Comment on the morphology of the erythrocytes.
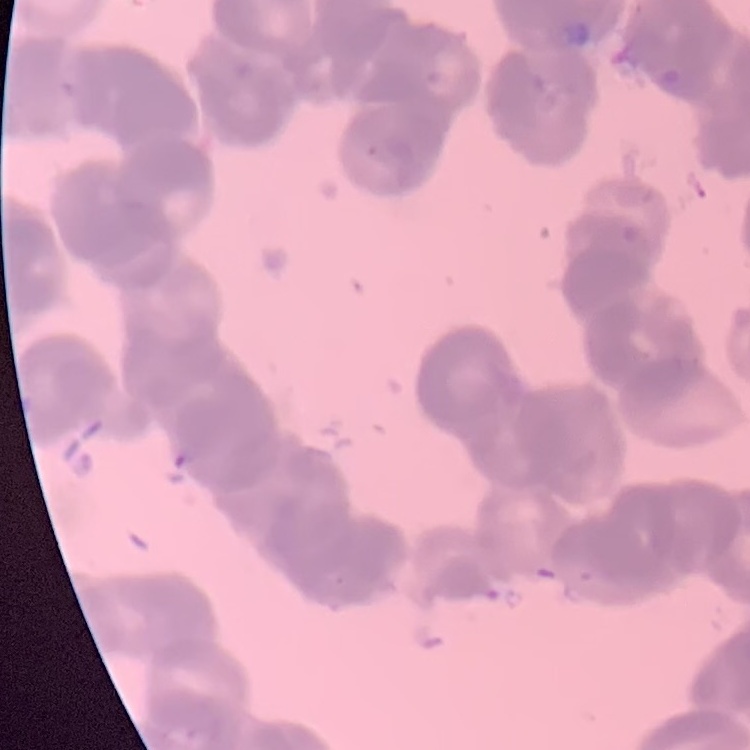
They show rouleaux formation.

stain: Field's or Giemsa
image_type: one tile cut from a larger photomicrograph
preparation: thin blood smear